Report the malaria status of this cell.
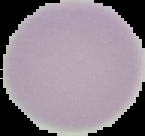

Uninfected.

Summary:
  - Preparation: thin blood film
  - Image type: segmented cell region with the area outside set to black
  - Image size: 145×136 pixels